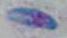

Summary:
  - Magnification: 1000x
  - Identification: Toxoplasma gondii
  - Modality: photomicrograph